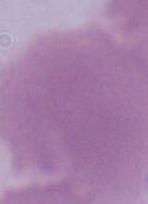
An erythrocyte is seen. 1000x magnification. Photomicrograph.